Assess this cell for malaria.
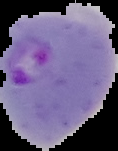

Parasitized.

image size = 118×151 pixels
image type = segmented cell region with the area outside set to black
preparation = thin blood film